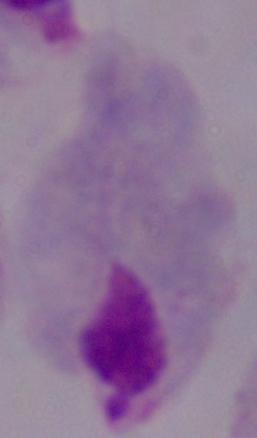
Summary:
  - Modality: photomicrograph
  - Identification: trichomonad
  - Magnification: 1000x